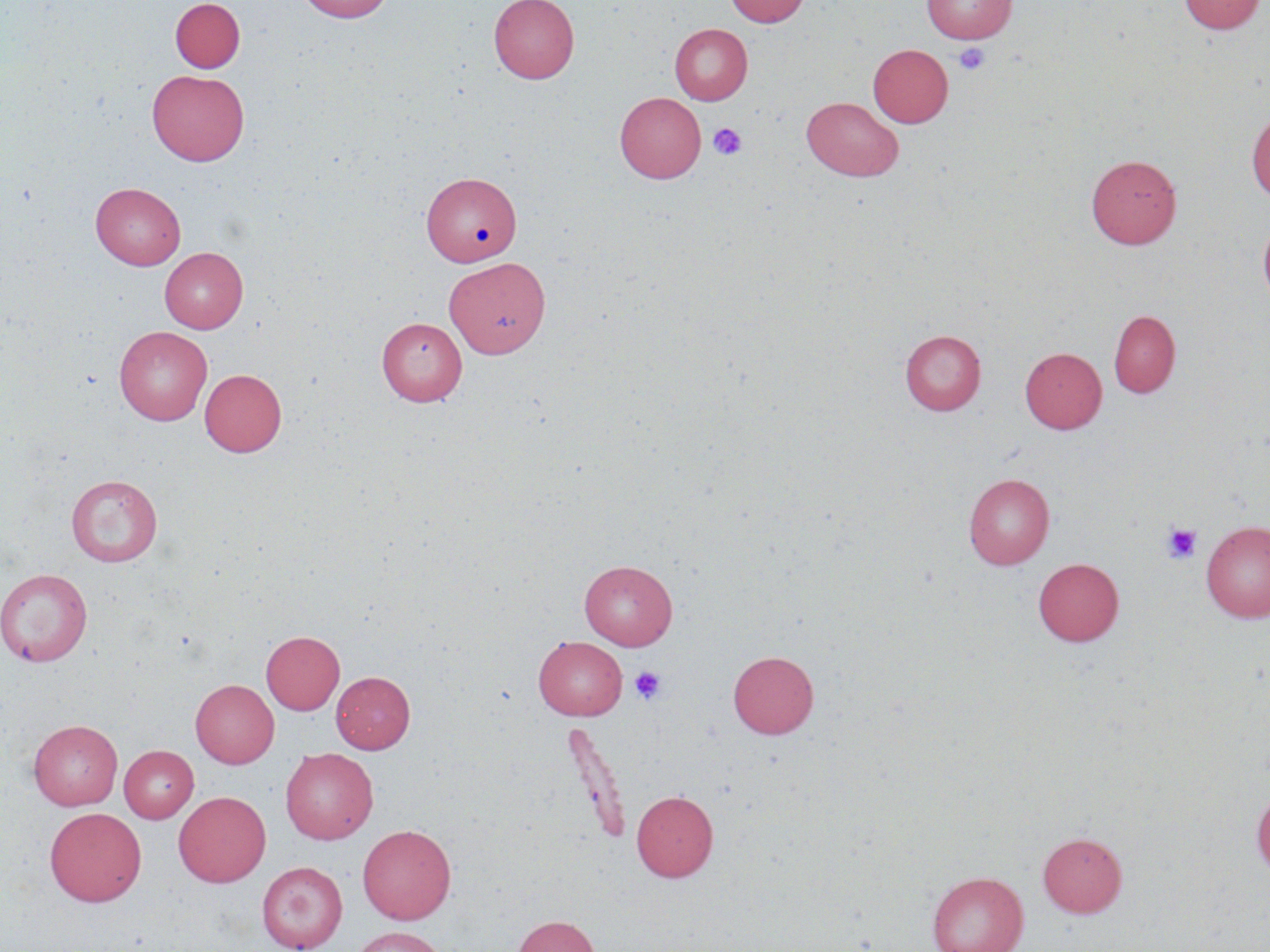
slide_level_diagnosis: no evidence of blood parasites
modality: optical microscopy
magnification: 1000x
field_of_view: single
uninfected_red_blood_cell_locations: 'approximate bounding boxes as (x1, y1, x2, y2) in pixels: (170, 0, 245, 73), (296, 0, 394, 23), (489, 0, 579, 84), (724, 0, 810, 27), (921, 0, 1017, 43), (1178, 0, 1266, 35), (670, 23, 752, 105), (868, 44, 953, 127), (147, 69, 250, 166), (615, 92, 706, 183), (801, 97, 904, 182), (1247, 107, 1270, 201), (1086, 154, 1182, 249), (421, 171, 521, 266), (90, 182, 186, 270), (1258, 215, 1270, 315), (160, 247, 248, 334), (444, 257, 550, 358), (1108, 310, 1180, 398), (376, 317, 467, 405), (114, 326, 212, 425), (900, 329, 986, 415), (1020, 347, 1107, 434), (199, 368, 287, 456), (962, 473, 1055, 570), (66, 474, 162, 566), (1200, 520, 1270, 623), (1033, 558, 1125, 646), (579, 559, 678, 650), (0, 568, 92, 666), (261, 631, 344, 715), (533, 636, 627, 720), (728, 650, 819, 739), (331, 671, 415, 753), (190, 679, 279, 768), (28, 719, 123, 810), (561, 720, 632, 846), (119, 745, 198, 823), (280, 747, 378, 844), (1251, 786, 1270, 879), (173, 790, 271, 887), (631, 790, 718, 881), (45, 807, 146, 906), (357, 824, 456, 924), (1038, 831, 1127, 918), (257, 861, 347, 951), (927, 871, 1028, 952), (513, 915, 601, 952), (350, 926, 448, 952)'
platelet_locations: 'approximate bounding boxes as (x1, y1, x2, y2) in pixels: (954, 43, 990, 75), (708, 122, 748, 160), (1160, 523, 1203, 564), (630, 665, 667, 705)'
preparation: thin blood smear
stain: May-Grünwald-Giemsa
image_size: 1270×952 pixels